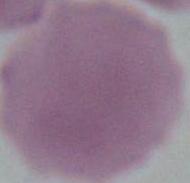

modality: photomicrograph
identification: red blood cell
magnification: 1000x